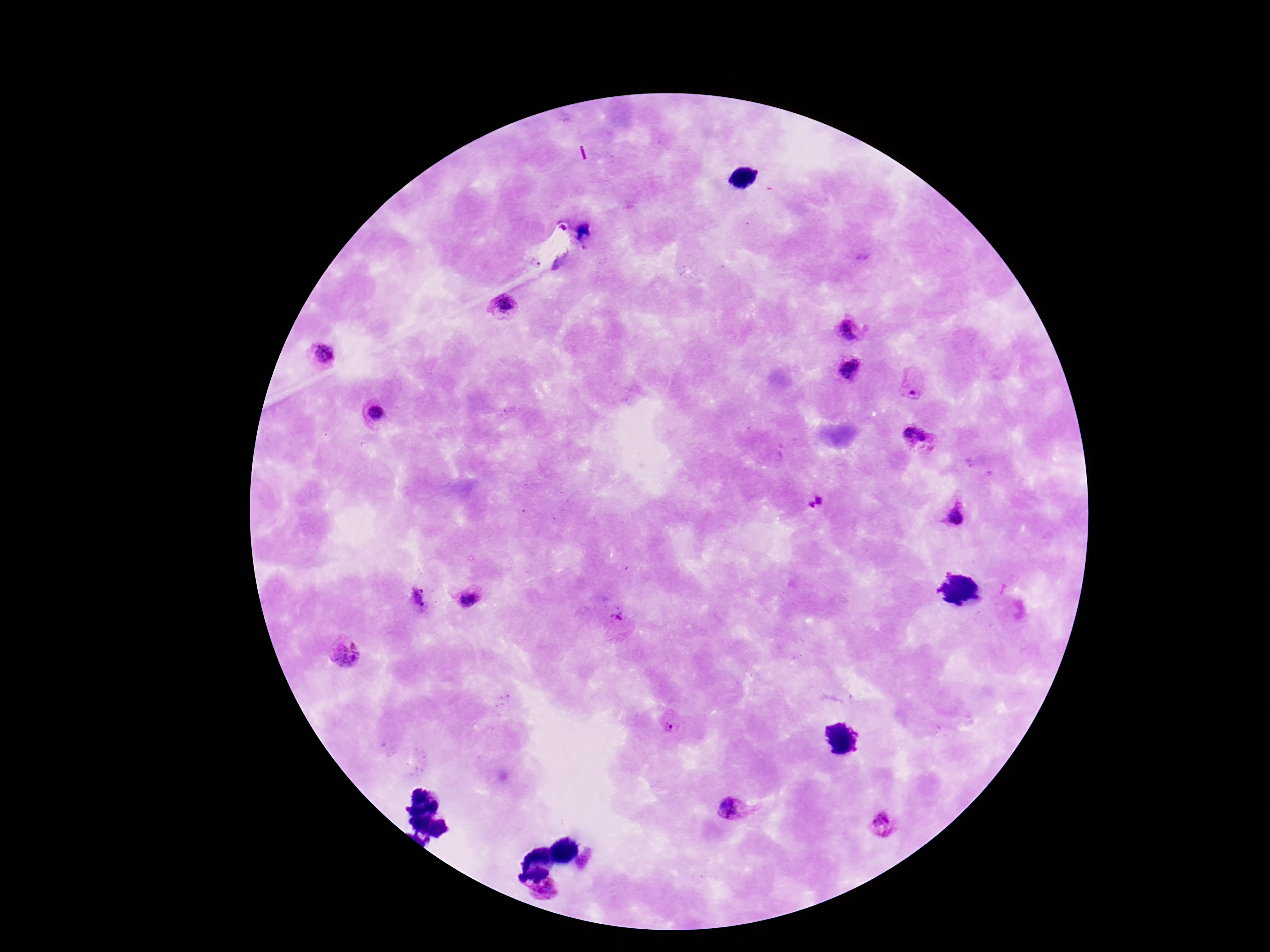 Approximate centers as (x, y) in pixels. Plasmodium parasite locations: (539, 264), (503, 304), (850, 330), (323, 354), (850, 368), (912, 388), (372, 411), (918, 439), (815, 501), (957, 516), (467, 597), (618, 620), (346, 651), (670, 720), (731, 809), (883, 823), (546, 893). Smartphone photograph taken through the microscope eyepiece. Thick blood film. Image is 1270×952 pixels. Giemsa stain. 100x magnification. Patient malaria status: positive. Single field of view.